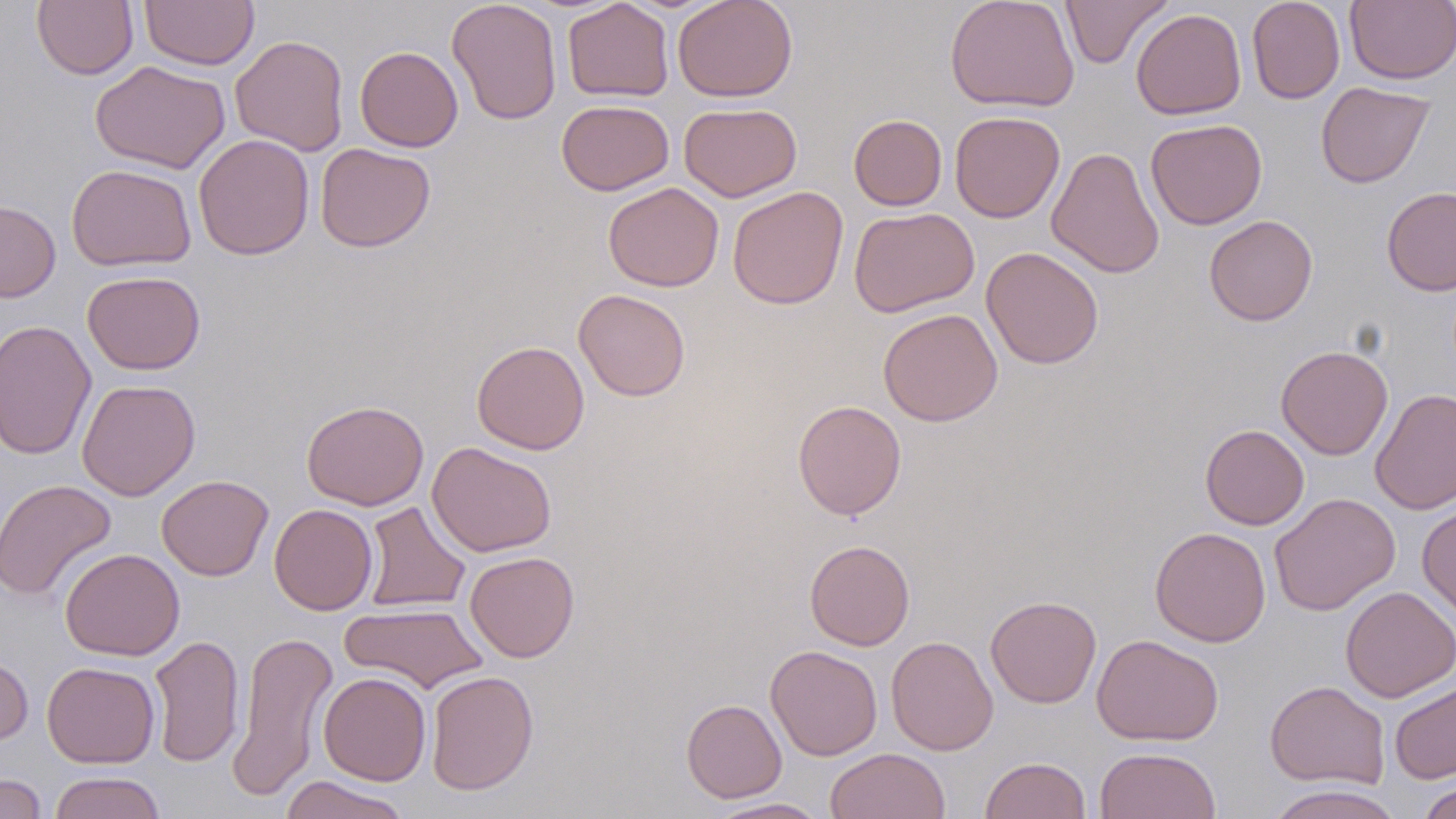

Approximate bounding boxes as (x1,y1)-(x2,y2) corner pairs in pixels. Uninfected red blood cell locations: (140,0)-(260,70), (446,0)-(562,125), (672,0)-(798,102), (945,0)-(1080,113), (1060,0)-(1173,69), (1247,0)-(1345,104), (32,1)-(138,80), (562,1)-(674,102), (1345,1)-(1456,85), (1131,8)-(1246,120), (230,34)-(350,156), (355,45)-(463,152), (91,60)-(230,173), (1316,81)-(1435,188), (556,99)-(674,195), (679,102)-(802,202), (950,111)-(1065,223), (849,114)-(948,211), (1145,119)-(1267,229), (193,134)-(314,260), (315,143)-(436,252), (1046,146)-(1165,279), (66,163)-(197,271), (603,182)-(724,292), (727,186)-(848,309), (1381,186)-(1456,296), (0,200)-(61,302), (848,207)-(980,317), (1204,215)-(1318,326), (981,247)-(1104,369), (82,270)-(205,375), (573,288)-(691,402), (878,308)-(1003,426), (0,319)-(97,461), (471,340)-(590,455), (1276,345)-(1394,459), (77,378)-(201,501), (1370,388)-(1456,515), (301,400)-(429,511), (793,400)-(906,520), (1200,424)-(1309,530), (427,441)-(557,558), (156,475)-(273,581), (0,479)-(118,602), (1270,493)-(1400,616), (361,501)-(471,613), (269,504)-(377,615), (1417,504)-(1456,624), (1150,526)-(1271,647), (804,539)-(915,651), (60,548)-(185,661), (465,551)-(580,662), (1340,586)-(1456,703), (985,595)-(1101,707), (340,602)-(488,693), (226,627)-(338,802), (148,634)-(245,768), (1091,634)-(1224,746), (886,635)-(998,756), (765,645)-(882,761), (0,650)-(34,750), (42,661)-(160,768), (425,670)-(539,795), (318,671)-(431,786), (1265,680)-(1390,789), (1389,680)-(1456,784), (681,698)-(787,802), (1094,747)-(1221,819), (825,748)-(951,819), (979,756)-(1091,819), (49,771)-(166,819), (0,773)-(47,819), (278,775)-(412,819), (1417,780)-(1456,819), (1262,785)-(1406,819), (706,797)-(831,818). Slide-level diagnosis: no evidence of blood parasites. Image is 1456×819 pixels. Thin blood smear. May-Grünwald-Giemsa-stained preparation. One field of a larger specimen. 1000x magnification. Optical microscopy.